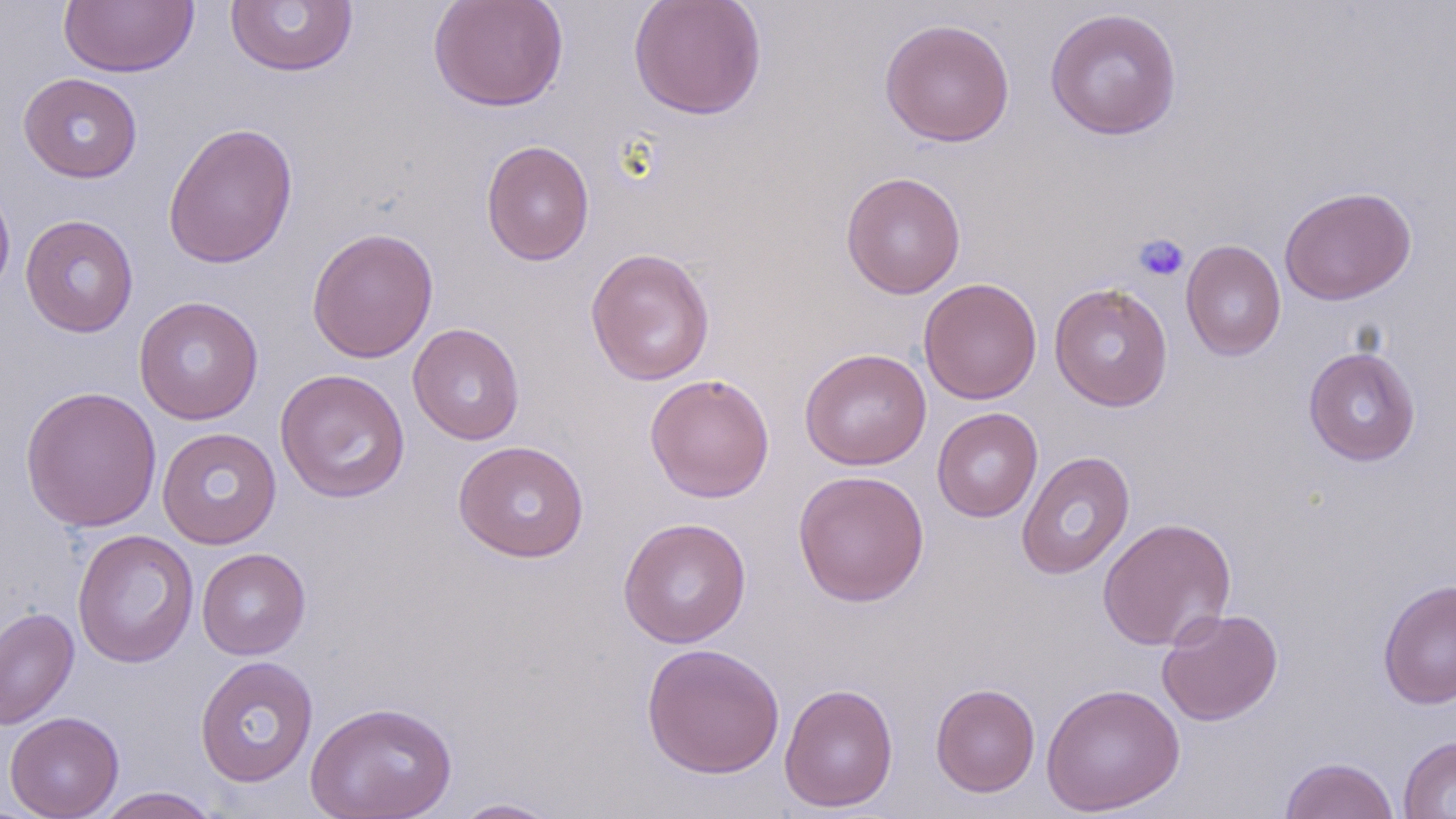

slide-level diagnosis = no evidence of blood parasites
platelet locations = approximate bounding boxes as (x1,y1)-(x2,y2) corner pairs in pixels: (1134,233)-(1190,282)
uninfected red blood cell locations = approximate bounding boxes as (x1,y1)-(x2,y2) corner pairs in pixels: (428,0)-(568,113), (628,0)-(767,120), (59,1)-(198,77), (225,1)-(358,77), (1044,7)-(1183,141), (880,17)-(1015,147), (18,72)-(143,183), (162,121)-(299,269), (481,140)-(595,266), (840,171)-(967,299), (0,173)-(16,303), (1279,186)-(1416,305), (20,214)-(139,337), (306,226)-(439,364), (1180,240)-(1286,361), (585,247)-(715,386), (918,277)-(1042,404), (1048,282)-(1174,411), (133,295)-(264,425), (408,323)-(524,445), (1303,346)-(1421,467), (799,348)-(931,470), (275,368)-(411,504), (644,373)-(775,503), (20,385)-(162,534), (931,407)-(1043,523), (157,427)-(282,549), (452,440)-(590,563), (1016,450)-(1135,580), (792,469)-(930,608), (1097,516)-(1237,652), (617,517)-(752,648), (72,529)-(199,668), (197,548)-(310,660), (1377,579)-(1456,710), (0,607)-(80,731), (1157,607)-(1283,726), (642,642)-(785,779), (195,656)-(319,787), (779,682)-(899,813), (930,682)-(1040,797), (1041,682)-(1185,815), (305,700)-(458,819), (4,711)-(124,818), (1398,736)-(1456,818), (1279,756)-(1400,819), (92,786)-(223,818), (449,797)-(564,818)
stain = May-Grünwald-Giemsa
field of view = one of a larger specimen
preparation = thin blood smear
image size = 1456×819 pixels
magnification = 1000x
modality = light microscopy